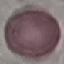

Malaria status: uninfected. Automatically extracted cell patch, resized to 64 × 64 pixels. Photographed with a smartphone camera at the microscope eyepiece. Giemsa-stained preparation. Thin blood smear.